State the blood parasite species.
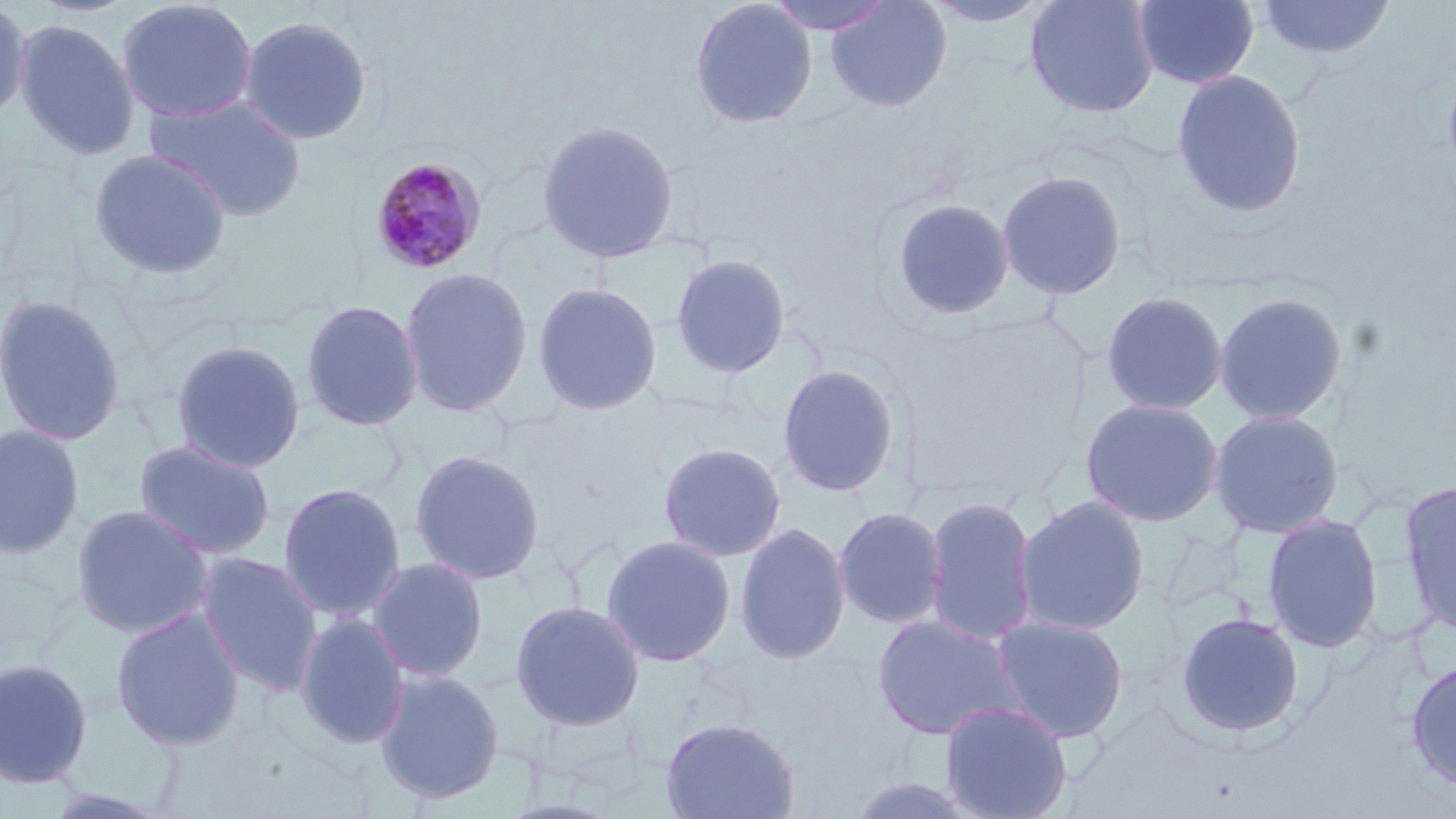

Plasmodium malariae.

{
  "uninfected_red_blood_cell_locations": "approximate bounding boxes as (x1,y1)-(x2,y2) corner pairs in pixels: (0,0)-(31,128), (115,0)-(258,124), (689,0)-(818,129), (764,0)-(896,36), (825,0)-(953,113), (920,0)-(1055,28), (1024,0)-(1160,119), (1132,0)-(1260,89), (1256,0)-(1396,62), (238,15)-(372,146), (13,17)-(141,160), (1441,57)-(1456,191), (1171,68)-(1307,218), (145,94)-(308,222), (537,119)-(679,263), (88,148)-(233,281), (997,169)-(1127,300), (887,197)-(1016,321), (670,253)-(792,379), (399,266)-(533,417), (532,281)-(663,416), (1100,290)-(1228,416), (1214,291)-(1348,426), (0,293)-(126,447), (300,299)-(424,431), (169,339)-(306,474), (776,363)-(901,498), (1080,397)-(1225,527), (1209,409)-(1345,538), (0,423)-(85,558), (133,439)-(276,561), (657,441)-(786,562), (408,448)-(546,585), (1398,479)-(1456,638), (277,482)-(406,622), (923,495)-(1040,646), (1013,495)-(1150,636), (71,503)-(214,638), (833,506)-(948,630), (1262,513)-(1383,653), (734,522)-(851,665), (600,534)-(736,667), (196,552)-(323,693), (366,555)-(489,682), (509,599)-(646,732), (111,607)-(245,751), (294,611)-(411,748), (1175,611)-(1305,739), (871,612)-(1023,741), (991,615)-(1129,743), (1404,657)-(1456,791), (0,658)-(94,789), (373,667)-(506,804), (939,700)-(1073,819), (660,716)-(800,819)",
  "image_size": "1456×819 pixels",
  "plasmodium_malariae_infected_red_blood_cell_locations": "approximate bounding boxes as (x1,y1)-(x2,y2) corner pairs in pixels: (369,156)-(487,276)",
  "stain": "May-Grünwald-Giemsa",
  "magnification": "1000x",
  "preparation": "thin blood smear",
  "modality": "optical microscopy",
  "field_of_view": "single"
}